Assess this cell for malaria.
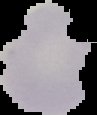
Uninfected.

{
  "image_type": "cell region segmented out of the field of view; surrounding area masked to black",
  "preparation": "thin blood film",
  "image_size": "97×115 pixels"
}